Classify this cell by malaria status.
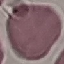

It is uninfected.

image_type: automatically extracted cell patch, resized to 64 × 64 pixels
preparation: thin smear
capture: smartphone through the microscope eyepiece
stain: Giemsa